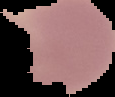
Image is 115×97 pixels. From a thin blood smear. Malaria status: parasitized. Segmented cell region on a black background.